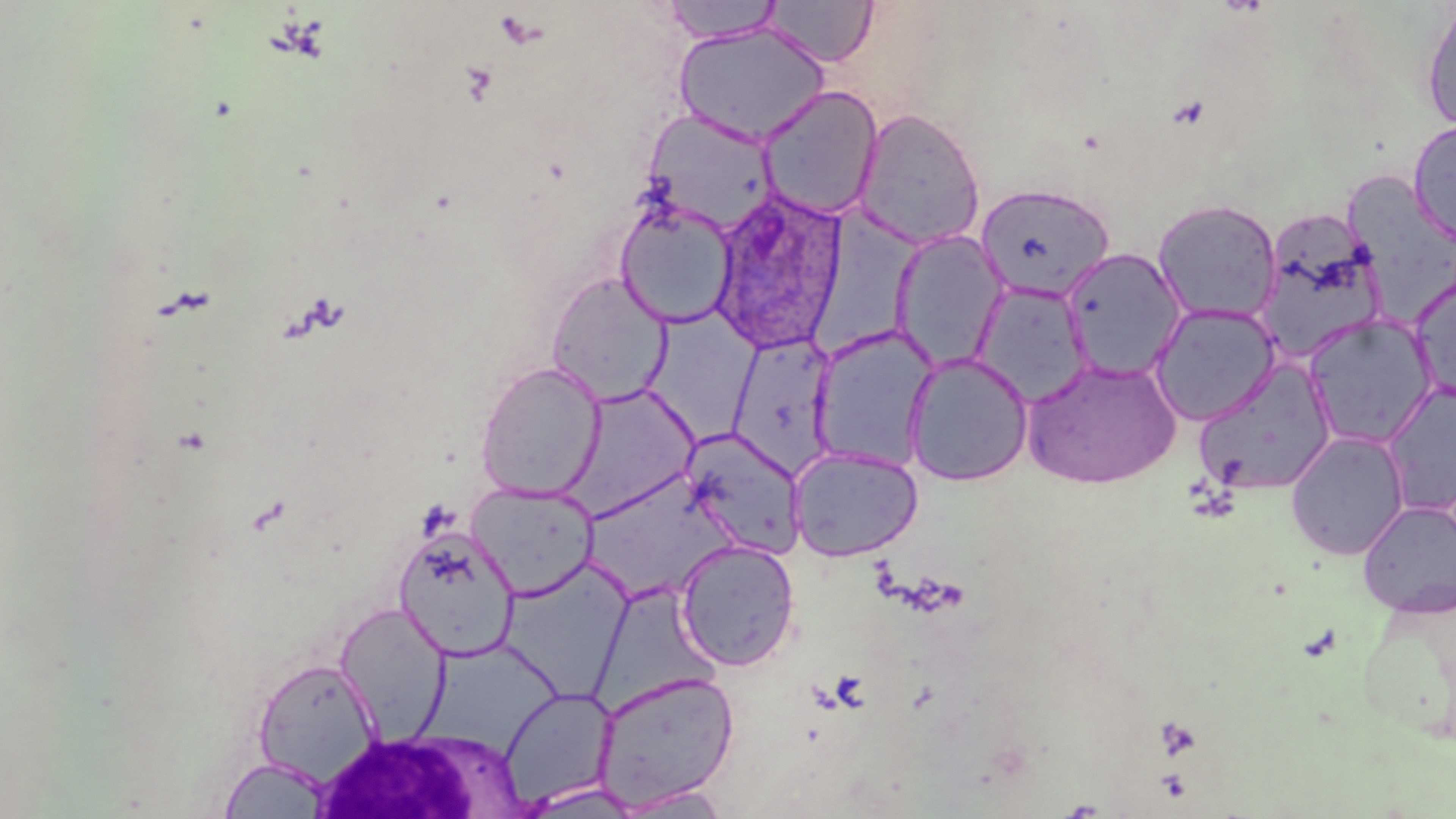

Summary:
  - Coordinate format: approximate bounding boxes as [x1, y1, x2, y2] in pixels
  - Uninfected red blood cell locations: [660, 1, 785, 44], [763, 1, 878, 67], [1420, 3, 1456, 134], [672, 22, 830, 147], [757, 85, 884, 221], [854, 108, 986, 250], [641, 109, 780, 236], [1408, 120, 1456, 246], [1344, 172, 1456, 319], [975, 183, 1115, 302], [1153, 199, 1282, 325], [615, 200, 738, 328], [811, 207, 918, 357], [1254, 215, 1388, 365], [890, 230, 1010, 371], [1060, 248, 1186, 380], [546, 272, 673, 406], [1410, 275, 1456, 404], [972, 282, 1093, 406], [1149, 303, 1282, 426], [647, 307, 767, 449], [1301, 312, 1438, 449], [809, 325, 939, 472], [727, 332, 840, 478], [904, 351, 1034, 487], [1022, 358, 1181, 489], [1193, 358, 1339, 497], [475, 362, 606, 501], [560, 382, 700, 520], [1380, 382, 1456, 518], [681, 427, 807, 558], [1285, 430, 1410, 561], [788, 446, 923, 562], [586, 474, 743, 602], [466, 481, 599, 600], [1357, 500, 1456, 619], [392, 524, 521, 660], [675, 538, 801, 671], [499, 558, 635, 700], [1358, 590, 1456, 746], [333, 602, 451, 741], [252, 658, 383, 786], [592, 670, 740, 811], [499, 686, 618, 810], [216, 758, 335, 818], [515, 782, 647, 818], [613, 785, 734, 818]
  - White blood cell locations: [314, 730, 522, 819]
  - Plasmodium ovale-infected red blood cell locations: [707, 187, 847, 354]
  - Slide-level diagnosis: Plasmodium ovale
  - Image size: 1456×819 pixels
  - Field of view: single
  - Modality: light microscopy
  - Magnification: 1000x
  - Preparation: thin blood smear
  - Stain: May-Grünwald-Giemsa